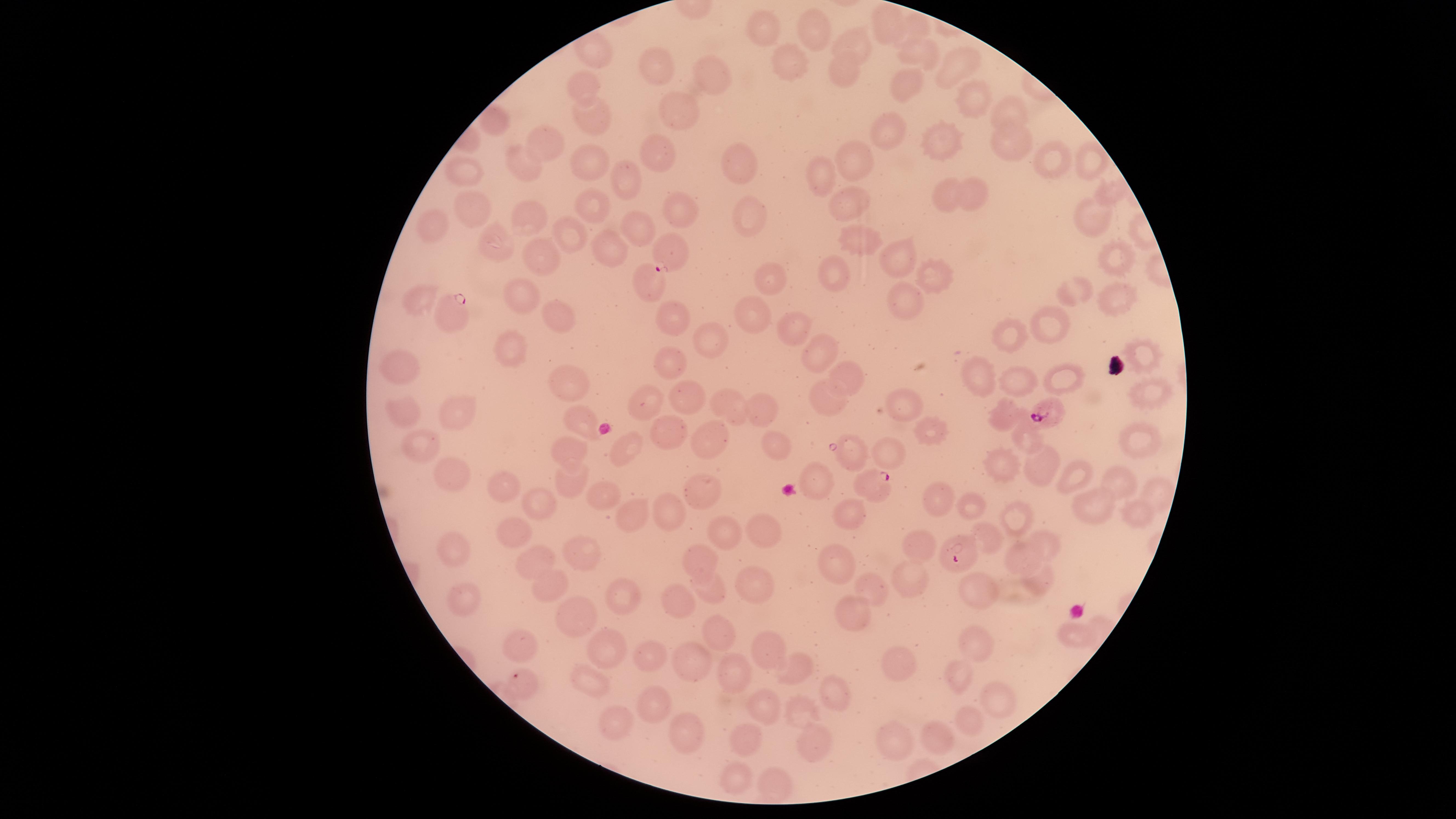

Approximate marker points as {x, y} in pixels.
Summary:
  - Uninfected red blood cells: {884, 22}, {917, 26}, {769, 27}, {815, 29}, {859, 39}, {923, 53}, {793, 59}, {660, 66}, {952, 67}, {843, 68}, {713, 73}, {899, 81}, {587, 87}, {977, 101}, {675, 113}, {1011, 116}, {592, 122}, {494, 123}, {880, 132}, {1009, 139}, {945, 142}, {547, 147}, {655, 150}, {728, 161}, {851, 163}, {1049, 165}, {1093, 167}, {523, 168}, {591, 169}, {823, 171}, {465, 174}, {622, 174}, {1110, 189}, {945, 193}, {968, 193}, {851, 202}, {478, 207}, {524, 209}, {750, 209}, {591, 210}, {681, 212}, {1089, 215}, {430, 229}, {641, 230}, {565, 232}, {854, 240}, {493, 247}, {612, 248}, {1116, 255}, {533, 260}, {896, 263}, {832, 273}, {936, 277}, {768, 282}, {649, 283}, {1082, 289}, {520, 295}, {420, 298}, {1105, 298}, {902, 305}, {568, 312}, {755, 312}, {671, 316}, {1048, 320}, {794, 330}, {1013, 334}, {712, 340}, {821, 345}, {511, 347}, {676, 356}, {1149, 357}, {401, 363}, {979, 366}, {850, 375}, {1064, 377}, {573, 379}, {1020, 386}, {1148, 393}, {680, 394}, {828, 394}, {651, 401}, {897, 402}, {732, 410}, {760, 410}, {1001, 411}, {397, 412}, {463, 418}, {583, 422}, {924, 428}, {1030, 432}, {672, 433}, {1140, 440}, {422, 442}, {708, 443}, {778, 444}, {616, 449}, {888, 449}, {846, 450}, {573, 452}, {1051, 452}, {997, 466}, {455, 475}, {1077, 476}, {1115, 476}, {572, 481}, {825, 481}, {601, 488}, {502, 493}, {1155, 494}, {708, 497}, {933, 497}, {1099, 500}, {976, 506}, {672, 509}, {542, 511}, {634, 512}, {1133, 513}, {1022, 515}, {851, 517}, {764, 528}, {517, 532}, {724, 534}, {994, 539}, {1051, 544}, {915, 545}, {456, 552}, {578, 555}, {1025, 556}, {702, 558}, {537, 559}, {841, 564}, {907, 576}, {1042, 576}, {549, 581}, {755, 582}, {875, 591}, {710, 592}, {968, 592}, {468, 594}, {682, 595}, {625, 603}, {854, 606}, {578, 612}, {1073, 633}, {724, 639}, {979, 642}, {522, 645}, {610, 648}, {766, 655}, {654, 660}, {907, 664}, {693, 665}, {955, 667}, {796, 675}, {736, 677}, {590, 680}, {835, 693}, {1000, 701}, {651, 702}, {762, 707}, {800, 708}, {963, 722}, {612, 729}, {689, 732}, {936, 738}, {896, 739}, {811, 743}, {743, 745}, {738, 784}, {776, 785}
  - Parasitized red blood cells: {670, 255}, {456, 315}, {1045, 411}, {873, 482}, {959, 556}, {522, 681}
  - Field of view: single
  - Presence: malaria parasites detected
  - Image size: 1456×819 pixels
  - Preparation: thin blood smear
  - Visible region: circular
  - Capture: smartphone photograph through the microscope eyepiece
  - Species: Plasmodium falciparum
  - Stain: Giemsa